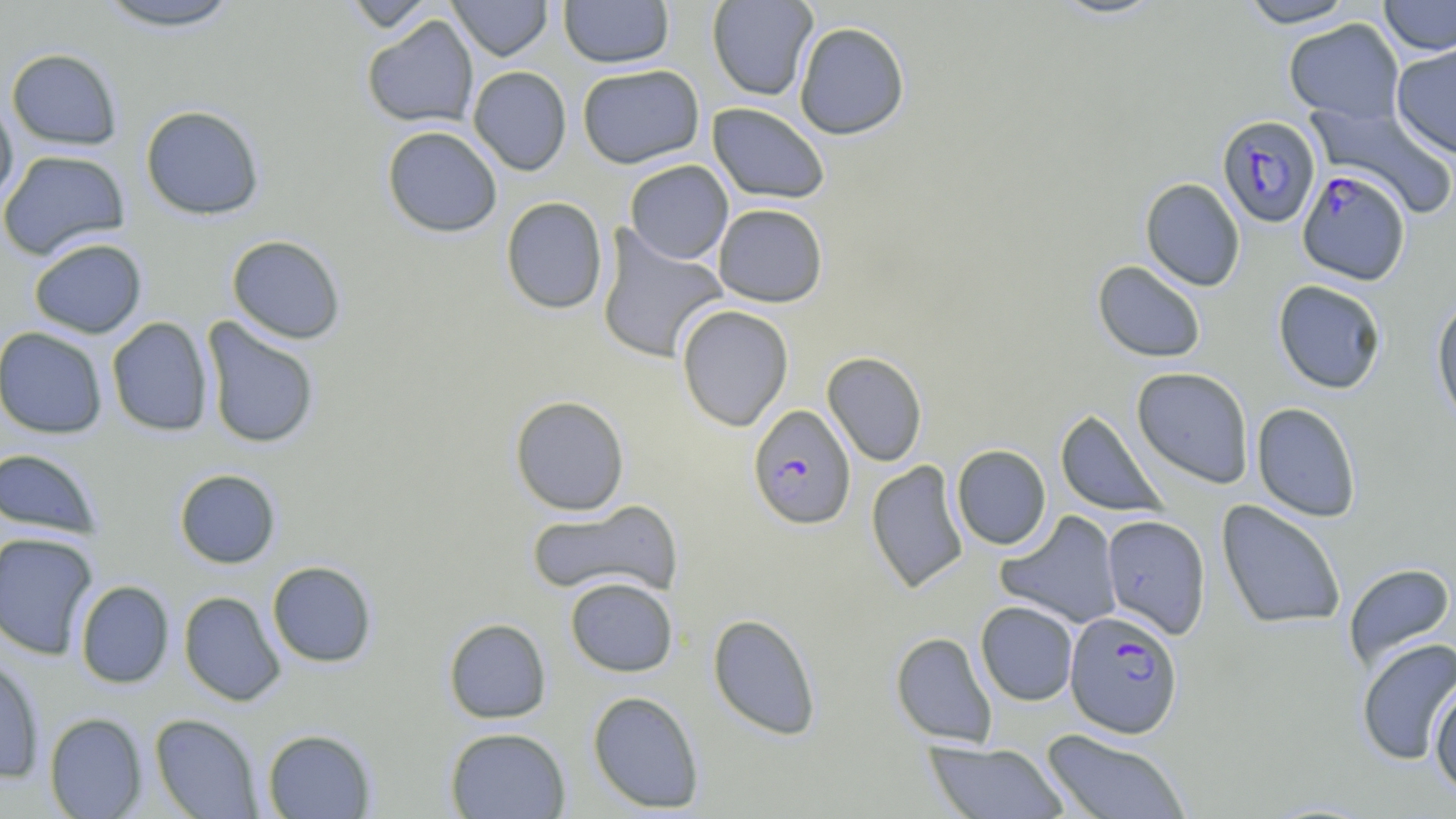 Approximate bounding boxes as (x1, y1, x2, y2) in pixels. Uninfected red blood cell locations: (92, 0, 246, 31), (341, 0, 438, 33), (447, 0, 553, 60), (558, 0, 674, 67), (707, 0, 818, 101), (1238, 0, 1357, 28), (1378, 0, 1456, 56), (361, 15, 479, 129), (1283, 18, 1405, 123), (794, 21, 910, 140), (1391, 43, 1456, 159), (6, 48, 123, 150), (577, 64, 704, 168), (468, 66, 572, 175), (0, 94, 19, 210), (1305, 101, 1455, 219), (707, 102, 831, 204), (140, 104, 265, 220), (382, 125, 503, 238), (0, 149, 130, 260), (624, 160, 733, 264), (1140, 177, 1245, 291), (500, 196, 608, 315), (713, 204, 828, 307), (596, 227, 728, 365), (226, 235, 347, 344), (28, 237, 147, 339), (1092, 260, 1207, 363), (1273, 279, 1388, 394), (1431, 295, 1456, 430), (676, 305, 794, 431), (106, 317, 214, 437), (201, 318, 321, 450), (0, 326, 108, 439), (822, 351, 928, 466), (1132, 367, 1254, 488), (509, 395, 630, 515), (1251, 402, 1362, 522), (1055, 409, 1168, 517), (951, 444, 1051, 550), (0, 448, 103, 538), (866, 459, 969, 593), (174, 468, 281, 569), (526, 500, 682, 600), (1216, 500, 1346, 630), (995, 510, 1122, 628), (1101, 514, 1211, 639), (0, 532, 99, 660), (267, 561, 377, 668), (1343, 563, 1456, 672), (565, 576, 678, 677), (75, 580, 174, 688), (179, 591, 287, 706), (976, 601, 1079, 706), (708, 613, 822, 740), (443, 618, 551, 724), (891, 631, 997, 747), (1356, 638, 1456, 766), (0, 655, 45, 784), (1428, 680, 1456, 797), (587, 691, 705, 813), (44, 712, 147, 818), (149, 713, 263, 818), (445, 727, 570, 818), (262, 728, 377, 818), (1040, 729, 1192, 819), (924, 741, 1070, 819). Plasmodium falciparum-infected red blood cell locations: (1217, 114, 1321, 228), (1298, 168, 1409, 284), (748, 405, 855, 529), (1064, 609, 1184, 739). Slide-level diagnosis: Plasmodium falciparum. Image is 1456×819 pixels. May-Grünwald-Giemsa stain. Light microscopy. 1000x magnification. Thin blood film. Single field of view.